Locate every Plasmodium falciparum-infected red blood cell.
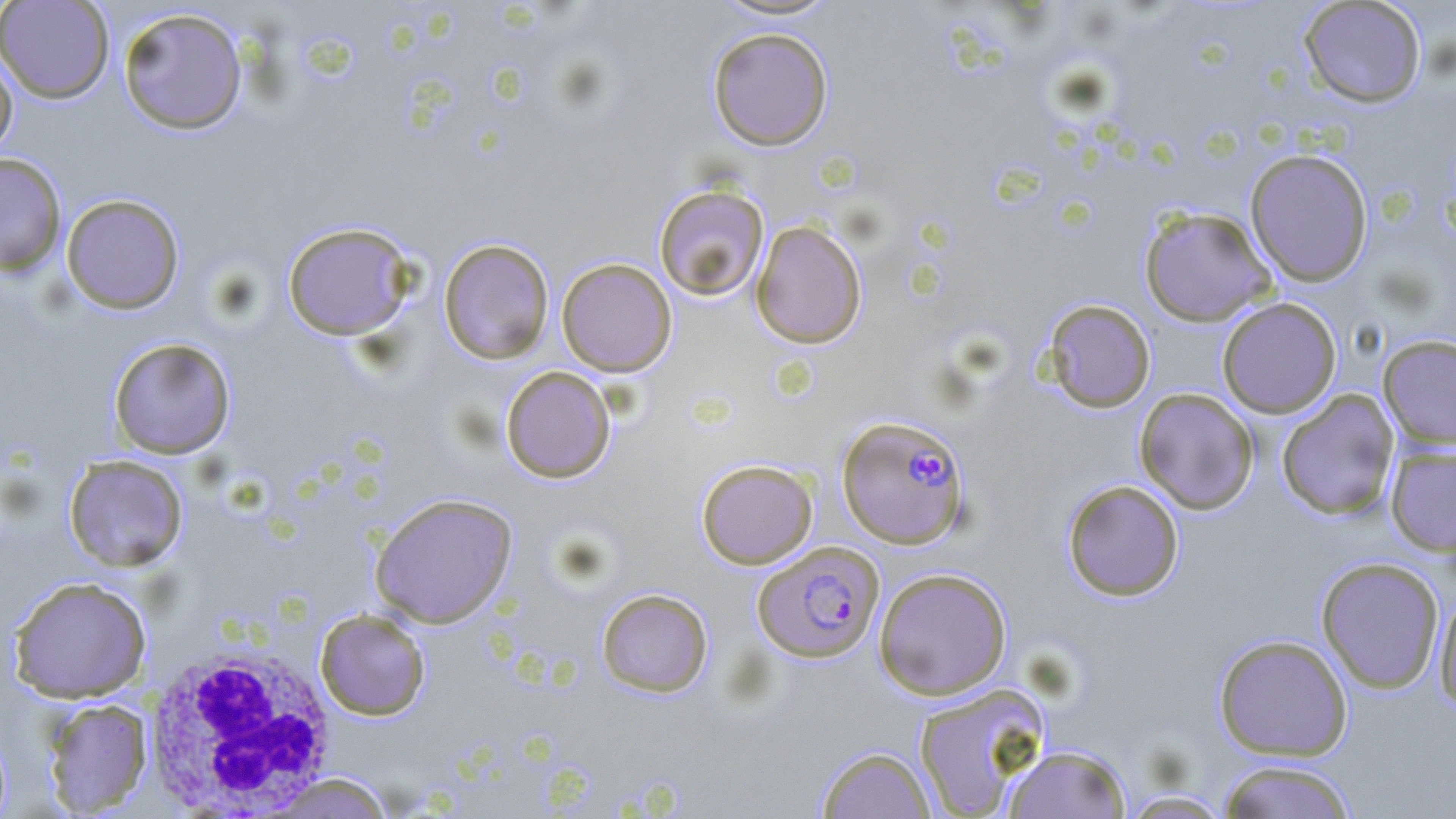
Approximate bounding boxes as (x1,y1)-(x2,y2) corner pairs in pixels.
Plasmodium falciparum-infected red blood cells: (837,414)-(970,548), (752,542)-(884,662).

Summary:
  - Uninfected red blood cell locations: (0,0)-(114,103), (709,0)-(843,22), (1298,0)-(1427,108), (117,6)-(248,135), (707,26)-(834,151), (0,49)-(18,159), (1245,148)-(1373,286), (0,152)-(67,276), (653,184)-(769,302), (60,193)-(184,314), (1139,206)-(1276,327), (751,220)-(867,348), (281,221)-(416,340), (438,238)-(554,365), (556,257)-(676,376), (1217,297)-(1342,418), (1043,298)-(1156,412), (1378,334)-(1456,449), (108,337)-(236,459), (500,366)-(616,483), (1134,388)-(1258,514), (1276,390)-(1400,521), (1385,445)-(1456,556), (63,454)-(188,572), (696,459)-(818,569), (1062,479)-(1185,601), (369,492)-(518,628), (1315,556)-(1445,693), (873,567)-(1012,699), (7,576)-(152,703), (1433,585)-(1456,711), (596,587)-(713,697), (315,609)-(430,720), (1213,633)-(1353,761), (913,683)-(1050,818), (41,698)-(153,816), (0,724)-(13,819), (1002,743)-(1132,818), (815,745)-(936,818), (1217,759)-(1359,819), (261,772)-(399,817), (1116,789)-(1237,818)
  - White blood cell locations: (143,642)-(338,813)
  - Slide-level diagnosis: Plasmodium falciparum
  - Preparation: thin blood smear
  - Magnification: 1000x
  - Stain: May-Grünwald-Giemsa
  - Field of view: single
  - Image size: 1456×819 pixels
  - Modality: optical microscopy